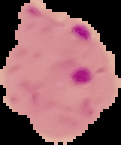

The area outside the segmented cell region is set to black. From a thin blood smear. Result: malaria parasites detected. Image is 121×145 pixels.